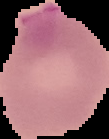
image type = segmented cell region with the area outside set to black
preparation = thin blood film
image size = 109×139 pixels
result = Plasmodium parasites detected